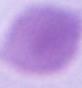
modality: micrograph
magnification: 1000x
identification: red blood cell